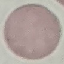
{
  "malaria_status": "uninfected",
  "image_type": "automatically extracted cell patch, resized to 64 × 64 pixels",
  "preparation": "thin smear",
  "stain": "Giemsa",
  "capture": "smartphone through the microscope eyepiece"
}